Classify this cell by malaria status.
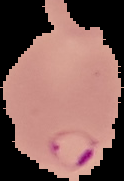
Parasitized.

image size = 124×181 pixels
preparation = thin blood smear
image type = cell region segmented out of the field of view; surrounding area masked to black